Name the blood parasite species.
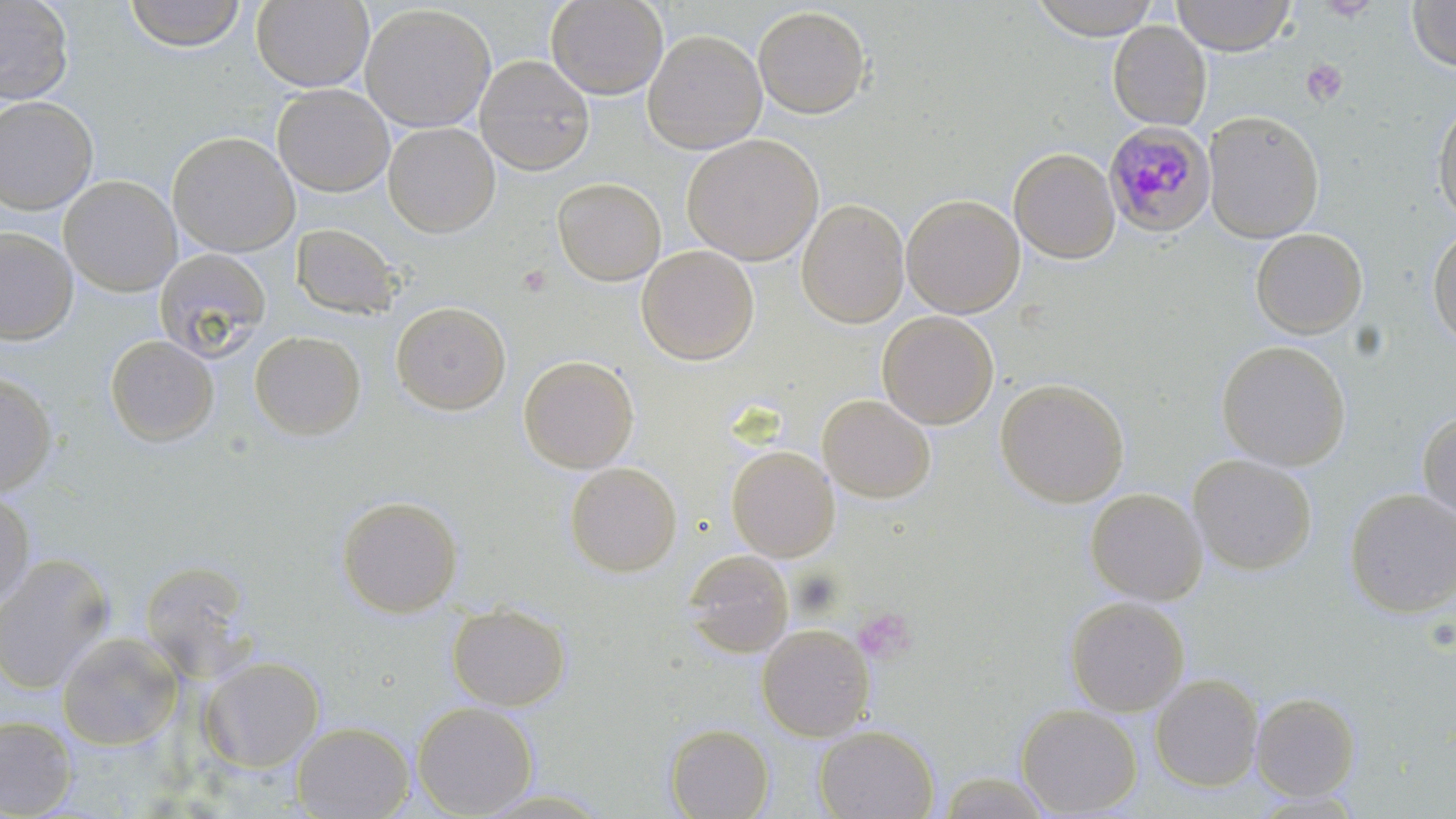

Plasmodium malariae.

{
  "field_of_view": "single",
  "uninfected_red_blood_cell_locations": "approximate bounding boxes as (x1,y1)-(x2,y2) corner pairs in pixels: (0,0)-(75,106), (124,0)-(247,52), (251,0)-(374,93), (545,0)-(669,100), (1031,0)-(1160,41), (1171,0)-(1294,55), (1407,1)-(1456,71), (359,4)-(496,134), (753,6)-(871,119), (1108,22)-(1212,131), (642,29)-(768,155), (475,55)-(595,176), (272,84)-(395,197), (0,97)-(99,215), (1432,97)-(1456,225), (1203,111)-(1324,243), (383,122)-(500,237), (166,131)-(300,257), (682,134)-(823,265), (1009,148)-(1121,264), (59,175)-(182,297), (552,177)-(666,286), (901,194)-(1024,318), (796,199)-(909,329), (290,223)-(402,320), (1427,224)-(1456,350), (0,228)-(77,345), (1250,228)-(1367,340), (636,245)-(759,365), (154,248)-(271,362), (390,301)-(511,416), (877,311)-(999,429), (249,330)-(366,441), (105,334)-(218,446), (1215,340)-(1351,470), (518,354)-(639,473), (0,371)-(57,497), (994,377)-(1129,508), (817,394)-(936,504), (1417,411)-(1456,525), (725,446)-(839,562), (1187,454)-(1317,575), (564,461)-(682,577), (1084,487)-(1207,605), (1344,488)-(1456,618), (0,492)-(36,607), (336,496)-(463,617), (682,550)-(794,659), (0,555)-(115,695), (139,559)-(256,680), (1064,597)-(1189,716), (447,604)-(571,711), (757,623)-(874,741), (56,631)-(183,750), (200,656)-(325,773), (1149,674)-(1264,792), (1250,692)-(1361,801), (412,701)-(538,818), (1015,704)-(1142,817), (0,715)-(76,817), (292,722)-(414,819), (814,723)-(939,819), (665,724)-(774,818), (471,789)-(615,818)",
  "stain": "May-Grünwald-Giemsa",
  "platelet_locations": "approximate bounding boxes as (x1,y1)-(x2,y2) corner pairs in pixels: (1301,58)-(1348,107), (517,264)-(552,296), (853,606)-(916,665)",
  "image_size": "1456×819 pixels",
  "magnification": "1000x",
  "plasmodium_malariae_infected_red_blood_cell_locations": "approximate bounding boxes as (x1,y1)-(x2,y2) corner pairs in pixels: (1103,122)-(1216,237)",
  "modality": "optical microscopy",
  "preparation": "thin blood film"
}